Give the extent of all uninfected red blood cells.
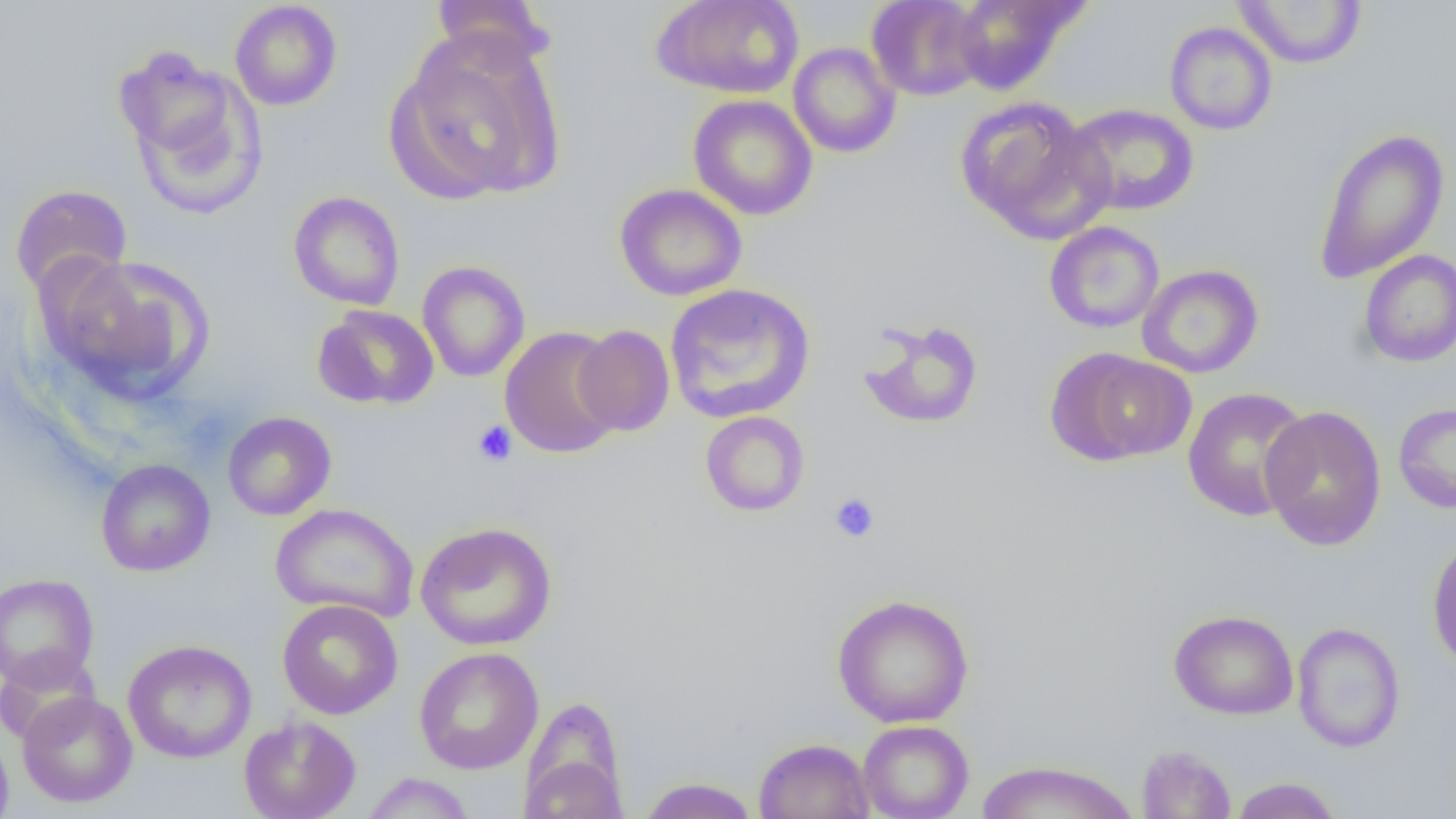
Approximate bounding boxes as (x1, y1, x2, y2) in pixels.
Uninfected red blood cells: (431, 0, 554, 72), (652, 0, 804, 99), (865, 0, 987, 101), (950, 0, 1084, 95), (1232, 0, 1367, 69), (229, 1, 342, 111), (1164, 21, 1277, 135), (391, 25, 567, 205), (788, 42, 902, 158), (112, 45, 259, 209), (688, 94, 818, 220), (955, 95, 1114, 244), (1064, 103, 1199, 216), (1312, 127, 1451, 283), (10, 184, 133, 299), (615, 184, 747, 302), (288, 191, 405, 310), (1044, 221, 1165, 334), (1358, 249, 1456, 367), (43, 253, 215, 404), (417, 260, 530, 382), (1137, 264, 1264, 378), (664, 283, 816, 423), (312, 304, 439, 410), (857, 317, 985, 430), (573, 324, 675, 436), (500, 326, 624, 459), (1053, 349, 1196, 465), (1182, 387, 1313, 522), (1393, 402, 1456, 514), (1259, 405, 1387, 551), (700, 411, 810, 517), (222, 412, 336, 520), (95, 459, 215, 576), (270, 503, 420, 622), (415, 521, 557, 651), (1427, 534, 1456, 675), (0, 573, 100, 690), (831, 593, 975, 729), (277, 599, 403, 719), (1168, 609, 1299, 720), (1292, 622, 1406, 753), (123, 639, 256, 763), (413, 647, 544, 774), (17, 690, 138, 808), (520, 701, 629, 817), (239, 715, 361, 819), (858, 719, 973, 819), (0, 723, 14, 819), (753, 738, 875, 819), (1136, 745, 1236, 818), (975, 760, 1141, 819), (361, 772, 476, 818), (637, 778, 761, 818), (1228, 778, 1343, 819).

Summary:
  - Platelet locations: (472, 420, 517, 467), (829, 492, 880, 543)
  - Slide-level diagnosis: no evidence of blood parasites
  - Image size: 1456×819 pixels
  - Field of view: one of a larger specimen
  - Preparation: thin blood film
  - Modality: optical microscopy
  - Magnification: 1000x